Find each parasitized RBC.
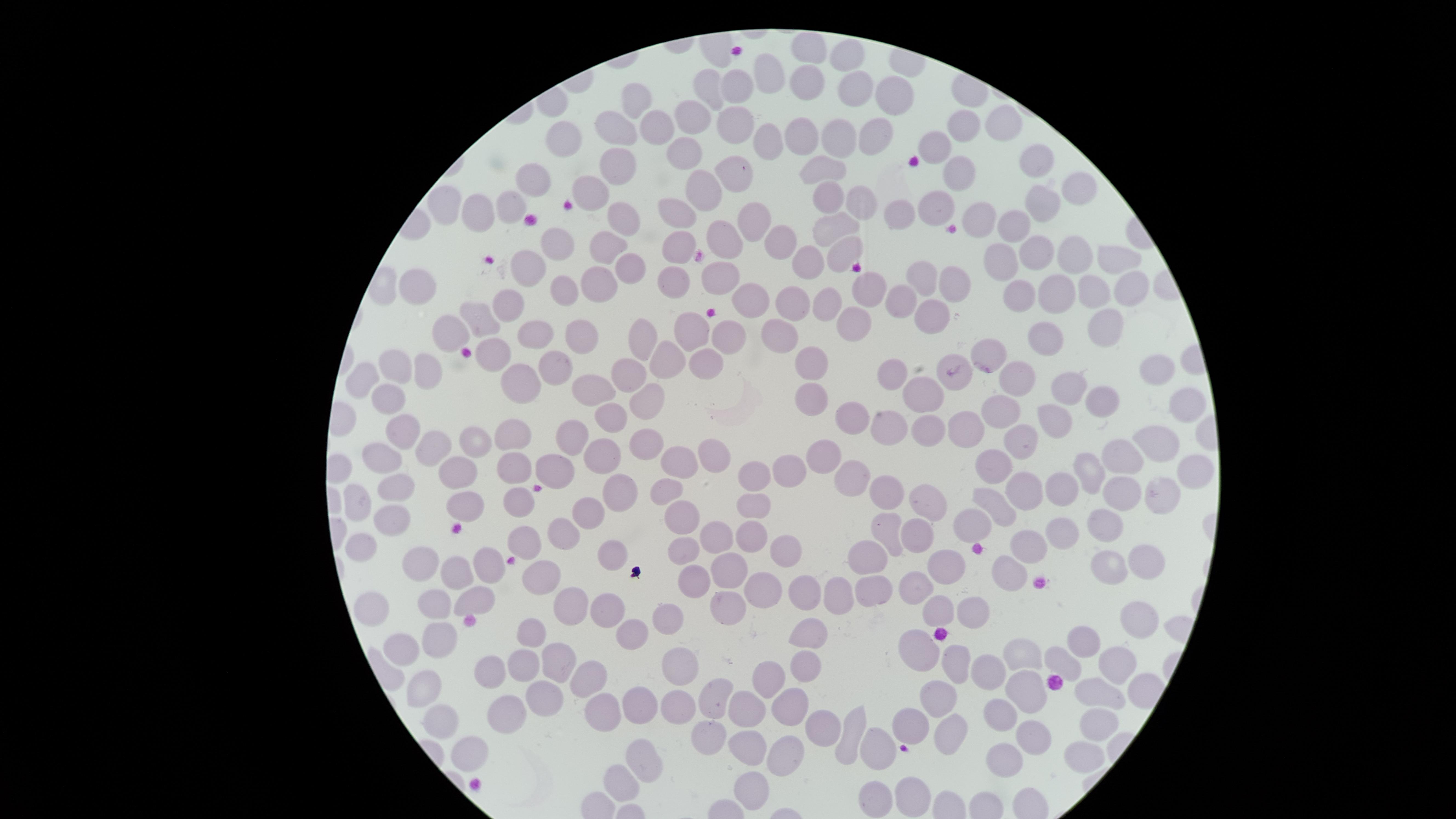
No parasitized RBCs identified.

field of view = single
visible region = circular
capture = smartphone photograph through the microscope eyepiece
uninfected RBCs = approximate marker points as (x, y) in pixels: (812, 49), (850, 60), (765, 75), (806, 83), (708, 85), (734, 87), (859, 90), (891, 94), (638, 100), (691, 114), (655, 119), (733, 121), (1006, 122), (621, 125), (960, 125), (878, 134), (805, 136), (569, 139), (838, 139), (771, 145), (937, 145), (687, 155), (1033, 160), (620, 167), (826, 169), (958, 170), (739, 172), (542, 175), (1078, 184), (591, 190), (707, 191), (826, 192), (865, 205), (1041, 205), (942, 207), (447, 209), (509, 209), (483, 212), (910, 212), (679, 214), (620, 219), (981, 219), (756, 222), (1016, 222), (834, 225), (725, 242), (560, 244), (776, 248), (1039, 251), (680, 252), (842, 252), (610, 256), (808, 259), (993, 259), (1073, 259), (1115, 260), (536, 266), (631, 269), (726, 278), (924, 278), (418, 280), (671, 281), (598, 282), (954, 282), (873, 284), (1129, 284), (1059, 290), (567, 291), (1090, 291), (1021, 295), (794, 299), (506, 301), (827, 302), (902, 303), (754, 306), (932, 317), (483, 320), (851, 325), (1107, 327), (455, 329), (583, 330), (696, 331), (780, 332), (730, 333), (534, 334), (1051, 334), (648, 337), (492, 352), (991, 353), (668, 355), (561, 363), (394, 364), (808, 366), (709, 367), (426, 369), (1159, 372), (894, 374), (959, 374), (1015, 375), (632, 376), (515, 380), (361, 382), (1066, 387), (598, 389), (810, 396), (920, 396), (389, 399), (1101, 400), (642, 402), (1180, 403), (1000, 408), (855, 418), (1055, 418), (610, 419), (891, 424), (924, 426), (967, 430), (405, 432), (513, 437), (575, 438), (1023, 440), (478, 443), (652, 443), (1156, 443), (431, 448), (830, 454), (714, 456), (604, 459), (381, 460), (1124, 460), (676, 463), (993, 464), (456, 467), (559, 467), (1094, 468), (513, 469), (1190, 469), (788, 470), (757, 475), (848, 476), (1022, 485), (1121, 486), (399, 489), (671, 489), (1057, 489), (1161, 490), (624, 491), (888, 495), (996, 497), (522, 499), (466, 503), (756, 503), (924, 503), (360, 505), (591, 512), (683, 515), (390, 519), (969, 525), (1107, 526), (564, 530), (884, 530), (913, 531), (712, 533), (750, 533), (1065, 533), (523, 540), (367, 541), (1029, 547), (682, 548), (777, 549), (613, 550), (871, 554), (1141, 556), (490, 560), (418, 562), (733, 567), (1112, 569), (465, 573), (938, 573), (1008, 573), (539, 574), (696, 579), (765, 588), (912, 590), (869, 591), (801, 593), (481, 595), (836, 595), (574, 597), (729, 604), (428, 606), (373, 607), (935, 609), (610, 611), (974, 611), (669, 616), (1139, 622), (531, 630), (632, 633), (808, 638), (1087, 642), (436, 643), (399, 646), (920, 649), (682, 656), (525, 657), (1018, 657), (561, 660), (1065, 660), (1119, 661), (806, 667), (991, 667), (495, 671), (957, 672), (586, 678), (774, 678), (432, 691), (1017, 692), (547, 694), (716, 697), (1102, 699), (936, 702), (641, 703), (678, 704), (788, 704), (750, 708), (508, 709), (603, 709), (1004, 713), (442, 721), (913, 724), (1099, 727), (823, 729), (710, 730), (953, 731), (853, 735), (1030, 737), (743, 747), (790, 748), (873, 750), (1084, 751), (475, 752), (642, 760), (1003, 760), (622, 782), (754, 785), (916, 794), (879, 797)
stain = Giemsa
preparation = thin blood smear
image size = 1456×819 pixels